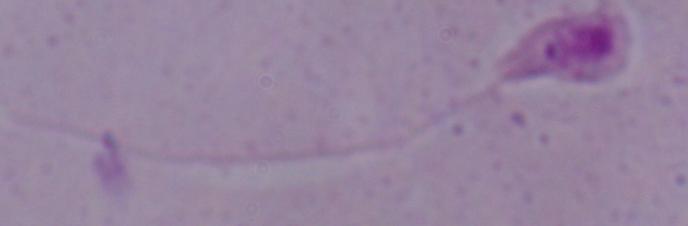
{
  "magnification": "1000x",
  "identification": "Leishmania",
  "modality": "photomicrograph"
}